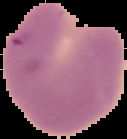 From a thin blood film. The area outside the segmented cell region is set to black. Result: Plasmodium parasites detected. Image is 127×139 pixels.